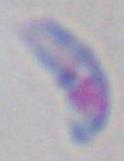

Summary:
  - Modality: micrograph
  - Magnification: 1000x
  - Identification: Toxoplasma gondii